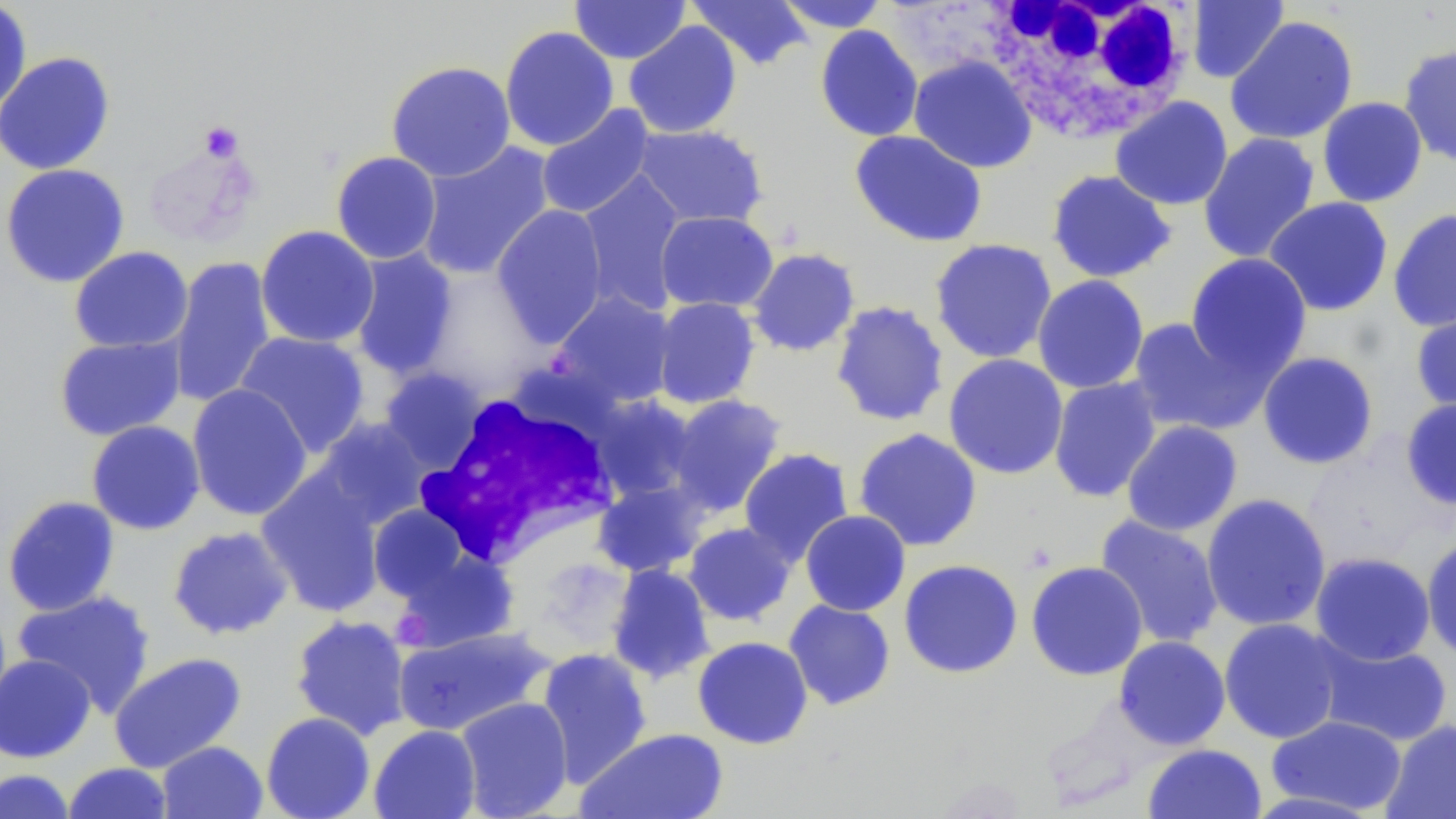
Summary:
  - Coordinate format: approximate bounding boxes as (x1, y1, x2, y2) in pixels
  - Uninfected red blood cell locations: (570, 0, 690, 64), (775, 0, 891, 32), (1186, 0, 1289, 83), (0, 1, 33, 120), (685, 1, 814, 71), (1225, 16, 1358, 145), (624, 20, 742, 139), (499, 25, 619, 151), (814, 25, 924, 142), (815, 39, 1035, 151), (1398, 43, 1456, 167), (0, 51, 116, 175), (909, 55, 1037, 173), (385, 60, 516, 182), (1110, 96, 1233, 210), (1317, 97, 1428, 207), (536, 104, 656, 220), (632, 123, 768, 228), (849, 130, 987, 248), (1198, 132, 1320, 263), (142, 141, 260, 249), (415, 141, 556, 281), (331, 151, 442, 264), (1, 164, 130, 288), (1046, 169, 1177, 283), (575, 170, 687, 316), (1263, 197, 1394, 317), (491, 204, 609, 348), (1387, 208, 1456, 332), (655, 210, 778, 313), (255, 225, 379, 348), (930, 238, 1057, 364), (69, 246, 193, 352), (746, 247, 860, 357), (348, 248, 459, 380), (1185, 253, 1312, 378), (168, 255, 276, 408), (419, 266, 549, 398), (1032, 275, 1149, 394), (551, 291, 678, 409), (651, 297, 761, 409), (830, 300, 949, 427), (1410, 303, 1456, 415), (1126, 315, 1270, 437), (234, 331, 371, 457), (54, 335, 185, 441), (1257, 351, 1379, 470), (943, 354, 1069, 480), (378, 367, 488, 472), (1048, 376, 1162, 503), (187, 384, 313, 521), (667, 394, 787, 516), (591, 395, 700, 503), (1400, 397, 1456, 510), (313, 417, 433, 527), (86, 420, 205, 535), (1121, 420, 1243, 537), (853, 428, 983, 552), (738, 448, 854, 565), (256, 469, 388, 617), (592, 479, 709, 577), (1201, 493, 1332, 632), (2, 495, 121, 617), (368, 505, 470, 602), (800, 510, 911, 616), (1094, 515, 1224, 650), (683, 521, 796, 626), (167, 526, 294, 640), (1421, 536, 1456, 663), (395, 549, 519, 652), (1310, 552, 1435, 665), (899, 559, 1023, 678), (1026, 561, 1148, 680), (606, 564, 716, 684), (12, 590, 156, 716), (783, 600, 896, 710), (290, 615, 412, 740), (1218, 618, 1345, 744), (392, 626, 552, 736), (692, 636, 813, 749), (1113, 636, 1231, 750), (1315, 638, 1453, 747), (535, 647, 653, 787), (108, 652, 247, 772), (0, 654, 96, 763), (455, 696, 574, 818), (261, 712, 375, 819), (1267, 715, 1408, 815), (1381, 720, 1456, 819), (368, 724, 481, 819), (577, 727, 729, 818), (157, 741, 268, 819), (1142, 743, 1267, 819), (62, 762, 174, 818), (0, 769, 76, 818)
  - White blood cell locations: (980, 0, 1197, 145), (378, 370, 489, 482), (412, 386, 625, 569)
  - Platelet locations: (200, 121, 243, 160)
  - Slide-level diagnosis: no evidence of blood parasites
  - Magnification: 1000x
  - Preparation: thin blood film
  - Modality: light microscopy
  - Field of view: single
  - Stain: May-Grünwald-Giemsa
  - Image size: 1456×819 pixels